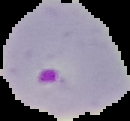
Summary:
  - Preparation: thin blood smear
  - Image type: cell region segmented out of the field of view; surrounding area masked to black
  - Malaria status: parasitized
  - Image size: 130×121 pixels